Outline each Plasmodium parasite.
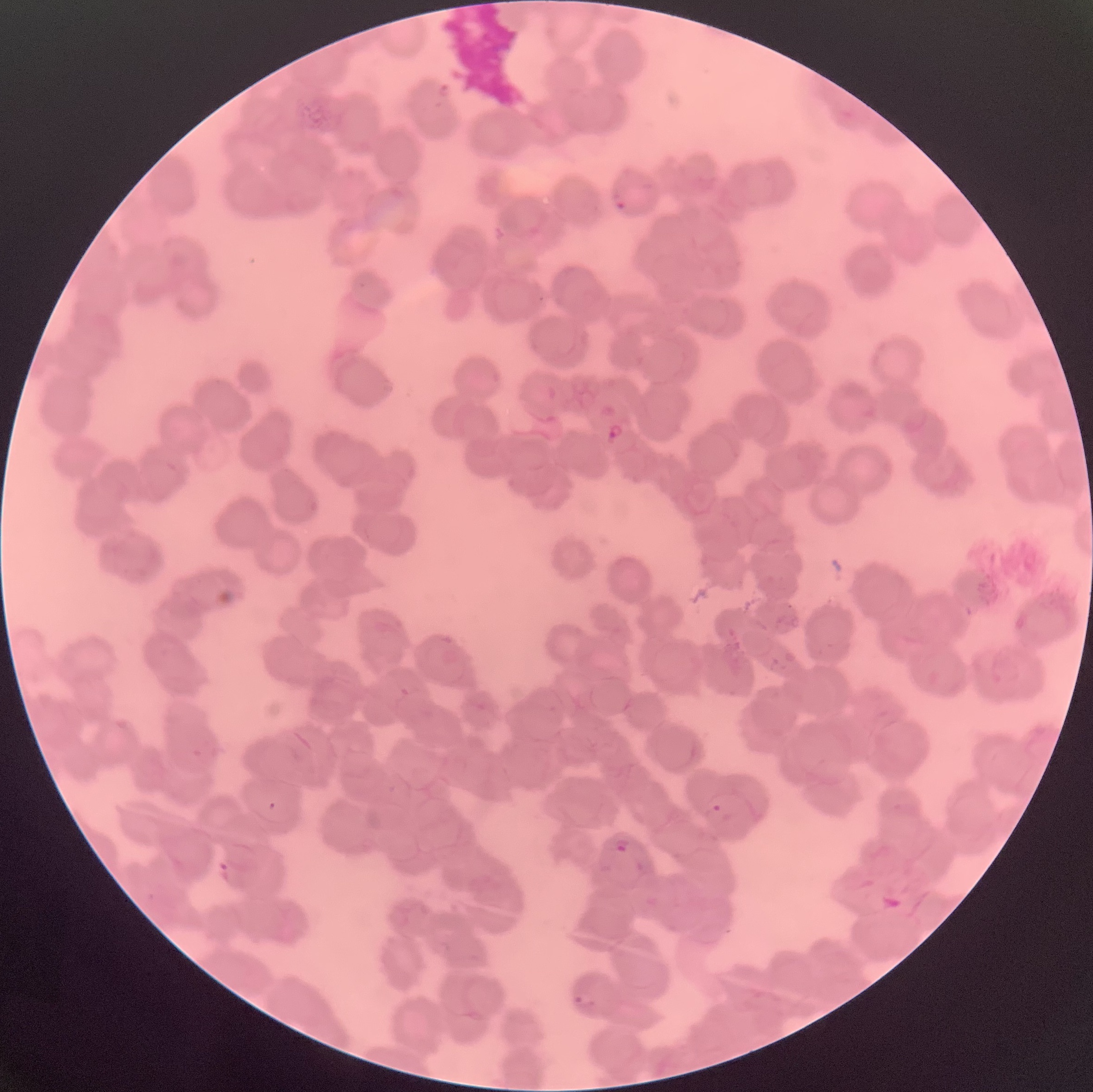

Approximate bounding boxes as (x1,y1)-(x2,y2) corner pairs in pixels.
Plasmodium parasites: (438,81)-(452,99), (613,198)-(627,211), (607,423)-(625,440), (270,801)-(275,811), (703,805)-(731,827), (614,836)-(630,855), (574,994)-(595,1007).

Summary:
  - Red blood cell morphology: rouleaux formation
  - Image size: 1093×1092 pixels
  - Modality: light microscopy
  - Preparation: thin blood film